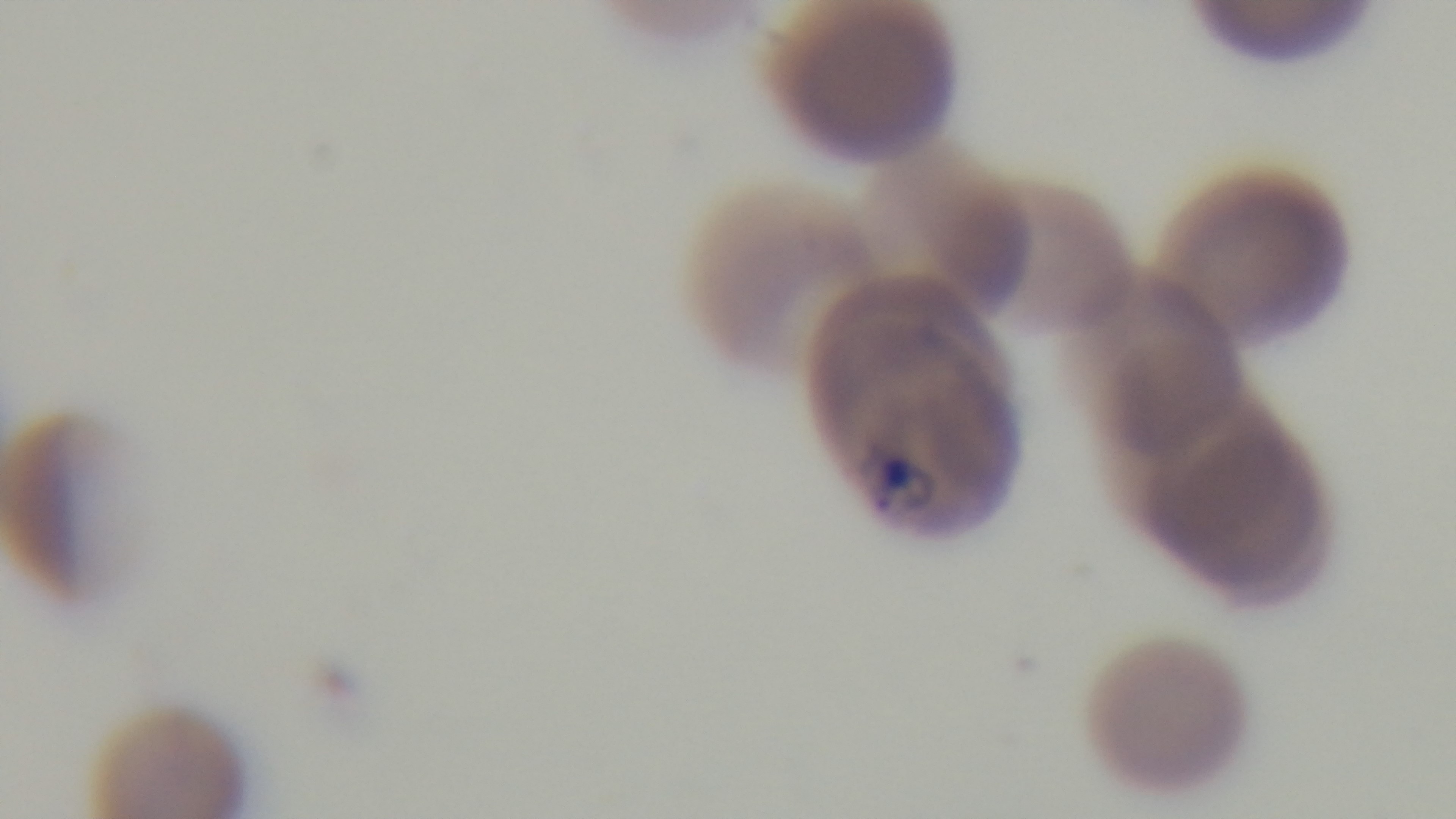

Summary:
  - Preparation: thin blood film
  - Capture: mounted 4K digital camera
  - Stain: Giemsa
  - Field of view: single
  - Modality: light microscopy
  - Malaria status: positive
  - Objective: 100x oil immersion